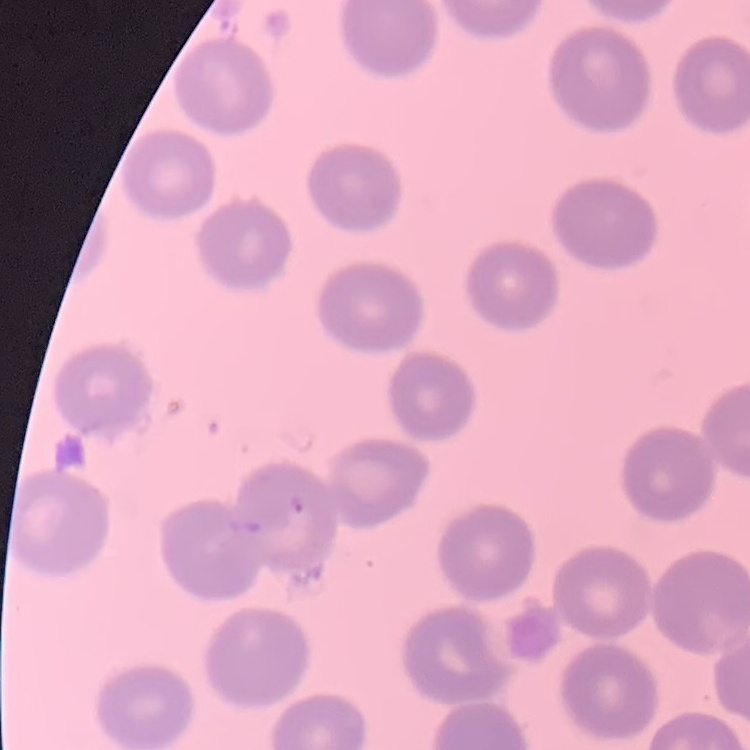
red blood cell morphology = no rouleaux formation
image type = one tile cut from a larger photomicrograph
preparation = thin blood smear
stain = Field's or Giemsa